Identify the blood parasite species.
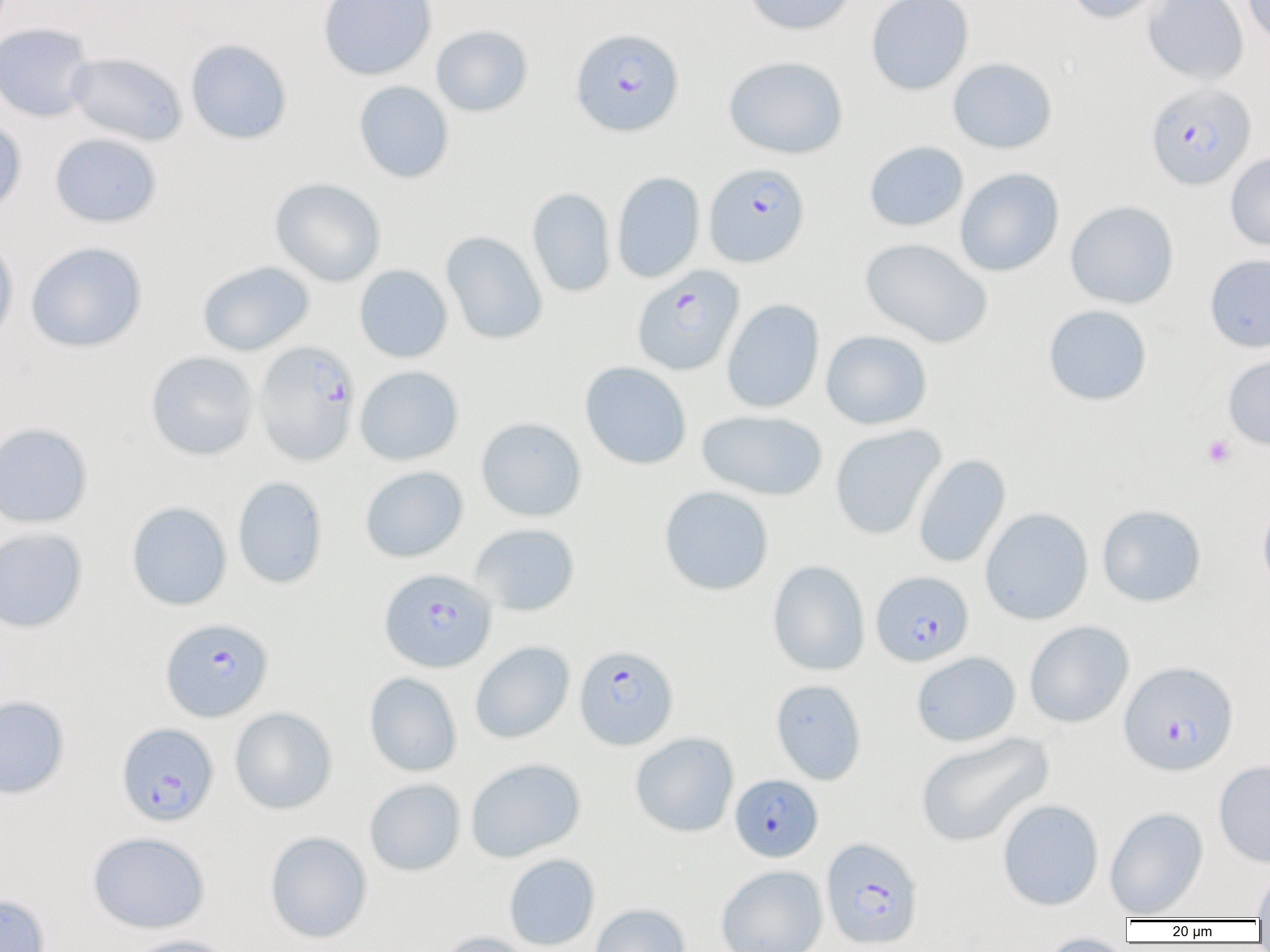

Plasmodium falciparum.

{
  "magnification": "1000x",
  "image_size": "1270×952 pixels",
  "preparation": "thin blood film",
  "plasmodium_falciparum_infected_red_blood_cell_locations": "approximate bounding boxes as (x1,y1)-(x2,y2) corner pairs in pixels: (570,28)-(684,137), (1145,82)-(1256,190), (704,162)-(809,267), (633,265)-(744,375), (254,341)-(360,466), (380,568)-(496,672), (871,571)-(974,666), (161,618)-(273,722), (574,645)-(678,750), (1119,661)-(1238,775), (116,722)-(218,826), (730,774)-(822,862), (821,837)-(923,949)",
  "platelet_locations": "approximate bounding boxes as (x1,y1)-(x2,y2) corner pairs in pixels: (1201,434)-(1236,469)",
  "modality": "optical microscopy",
  "uninfected_red_blood_cell_locations": "approximate bounding boxes as (x1,y1)-(x2,y2) corner pairs in pixels: (318,0)-(436,80), (743,0)-(856,35), (866,0)-(974,95), (1064,0)-(1168,24), (1143,0)-(1249,84), (1243,0)-(1270,50), (0,23)-(96,123), (431,25)-(533,117), (185,39)-(292,145), (65,52)-(187,146), (723,55)-(848,159), (948,57)-(1057,154), (354,81)-(454,183), (0,117)-(27,215), (49,133)-(162,228), (864,140)-(969,232), (1225,151)-(1270,251), (955,168)-(1064,276), (612,171)-(705,284), (269,177)-(386,287), (527,187)-(616,297), (1065,200)-(1179,309), (441,231)-(547,345), (0,234)-(18,348), (860,237)-(993,348), (25,242)-(147,353), (1205,254)-(1270,352), (197,261)-(314,356), (354,265)-(452,363), (722,298)-(824,413), (1043,304)-(1152,406), (821,330)-(932,430), (145,350)-(259,461), (1222,351)-(1270,451), (580,361)-(691,469), (355,365)-(464,465), (696,409)-(828,501), (476,417)-(586,521), (0,422)-(93,529), (830,424)-(947,540), (913,454)-(1011,569), (360,466)-(468,563), (232,476)-(327,589), (659,486)-(774,595), (126,501)-(232,610), (1258,501)-(1270,600), (1097,505)-(1206,607), (980,507)-(1093,625), (470,523)-(580,616), (0,527)-(88,633), (767,560)-(870,676), (1024,621)-(1134,728), (470,641)-(574,743), (911,651)-(1021,746), (365,672)-(462,777), (770,679)-(867,785), (0,695)-(70,799), (230,707)-(337,814), (631,732)-(739,837), (914,732)-(1053,847), (465,758)-(586,863), (1214,759)-(1270,867), (364,779)-(465,876), (997,799)-(1104,911), (1105,807)-(1208,918), (87,831)-(210,934), (265,831)-(372,943), (503,853)-(600,951), (716,865)-(828,952), (1252,865)-(1270,921), (0,893)-(50,952), (589,903)-(691,952), (434,931)-(538,952), (1036,932)-(1133,952), (124,934)-(239,952)",
  "field_of_view": "one of a larger specimen"
}